Name the blood parasite species.
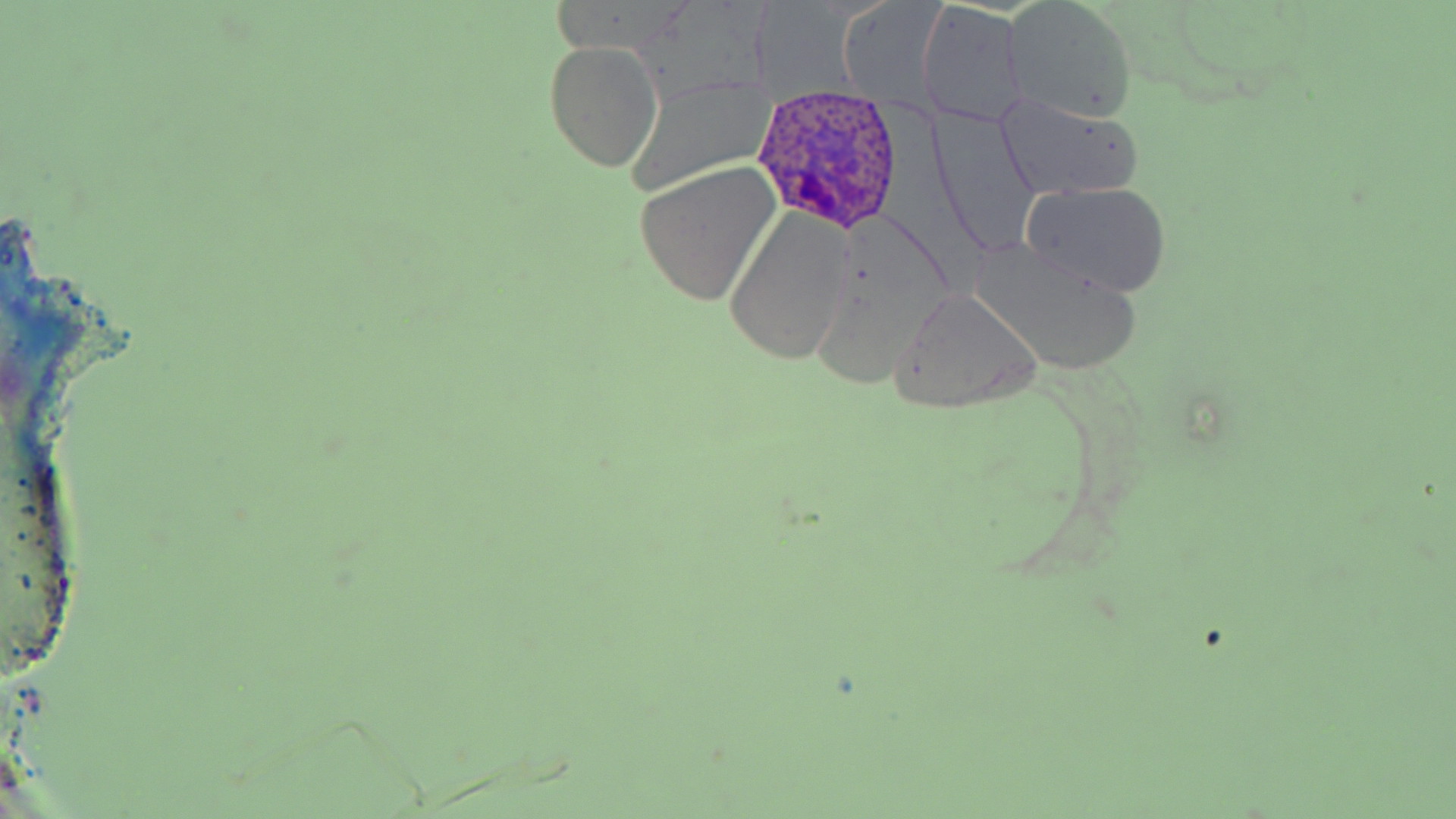

Plasmodium ovale.

Approximate bounding boxes as (x1, y1, x2, y2) in pixels. Uninfected red blood cell locations: (1004, 0, 1140, 123), (836, 3, 952, 113), (915, 6, 1026, 126), (544, 41, 663, 173), (626, 76, 770, 196), (995, 93, 1142, 201), (633, 162, 781, 306), (1020, 181, 1173, 299), (725, 210, 852, 365), (970, 239, 1140, 377), (890, 288, 1044, 412). Plasmodium ovale-infected red blood cell locations: (755, 89, 904, 235). Optical microscopy. Thin blood smear. Image is 1456×819 pixels. Single field of view. May-Grünwald-Giemsa stain. 1000x magnification.